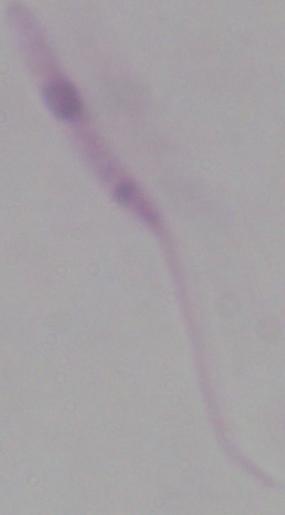 A Leishmania parasite is shown. Photomicrograph. 1000x magnification.